Name the parasite shown.
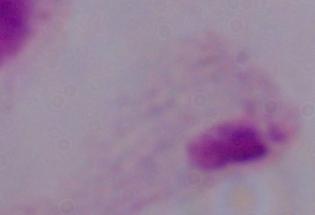

This is a trichomonad.

Captured at 1000x magnification. Micrograph.